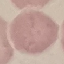 Result: no malaria parasites detected. Thin blood film. Cell patch, automatically extracted from a larger field of view and resized to 64 × 64 pixels. Photographed with a smartphone camera at the microscope eyepiece. Giemsa stain.